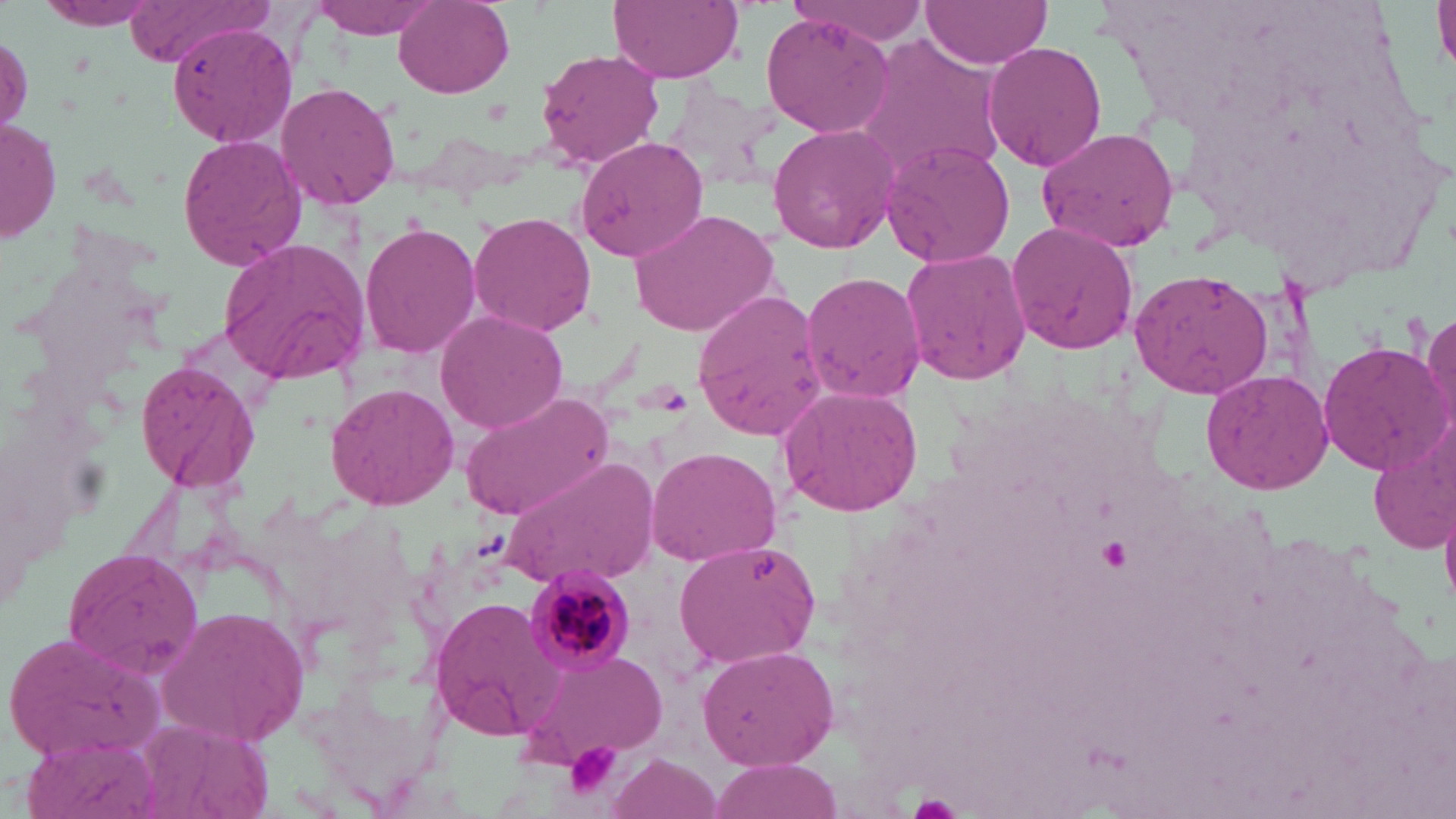

slide-level diagnosis = Plasmodium malariae
magnification = 1000x
field of view = single
modality = light microscopy
platelet locations = approximate bounding boxes as (x1, y1, x2, y2) in pixels: (563, 740, 623, 798)
image size = 1456×819 pixels
Plasmodium malariae-infected red blood cell locations = approximate bounding boxes as (x1, y1, x2, y2) in pixels: (523, 563, 634, 675)
uninfected red blood cell locations = approximate bounding boxes as (x1, y1, x2, y2) in pixels: (30, 0, 165, 32), (126, 0, 278, 67), (307, 0, 446, 37), (391, 0, 515, 98), (608, 0, 744, 82), (783, 0, 936, 44), (1431, 0, 1456, 76), (919, 1, 1054, 69), (760, 13, 893, 135), (167, 29, 299, 154), (849, 33, 1009, 185), (0, 34, 32, 145), (982, 39, 1107, 173), (534, 48, 665, 169), (275, 81, 402, 210), (1, 118, 62, 245), (766, 123, 898, 252), (1036, 125, 1182, 252), (177, 133, 307, 273), (575, 134, 711, 267), (879, 138, 1017, 268), (627, 206, 780, 337), (468, 210, 597, 335), (1006, 218, 1140, 357), (362, 219, 483, 359), (217, 237, 374, 384), (899, 245, 1033, 388), (1129, 266, 1278, 397), (801, 271, 926, 402), (691, 284, 828, 440), (1423, 305, 1456, 435), (433, 308, 569, 434), (1317, 338, 1450, 474), (134, 358, 259, 495), (1200, 368, 1335, 495), (326, 382, 459, 510), (775, 383, 925, 516), (460, 389, 617, 522), (1367, 415, 1456, 555), (646, 444, 783, 567), (505, 453, 661, 589), (675, 537, 822, 668), (64, 547, 206, 677), (427, 596, 564, 743), (153, 605, 312, 748), (6, 630, 162, 762), (696, 642, 841, 773), (519, 648, 672, 769), (135, 717, 275, 819), (18, 730, 160, 819), (603, 754, 723, 819), (709, 758, 843, 817)
preparation = thin blood smear
stain = May-Grünwald-Giemsa